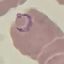

Summary:
  - Result: malaria parasites identified
  - Image type: automatically extracted cell patch, resized to 64 × 64 pixels
  - Stain: Giemsa
  - Capture: smartphone through the microscope eyepiece
  - Preparation: thin blood film